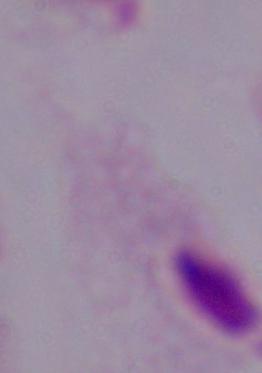
Summary:
  - Magnification: 1000x
  - Identification: trichomonad
  - Modality: micrograph